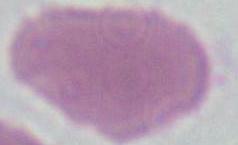

Summary:
  - Magnification: 1000x
  - Identification: erythrocyte
  - Modality: photomicrograph